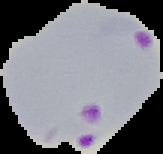
image type = cell region segmented out of the field of view; surrounding area masked to black
result = malaria parasites detected
image size = 163×154 pixels
preparation = thin blood smear